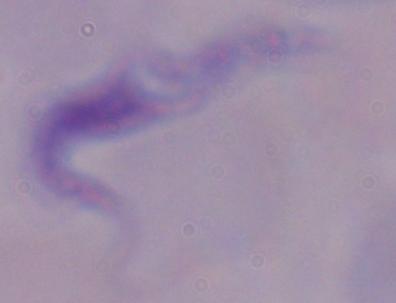 A trypanosome is shown. Captured at 1000x magnification. Micrograph.